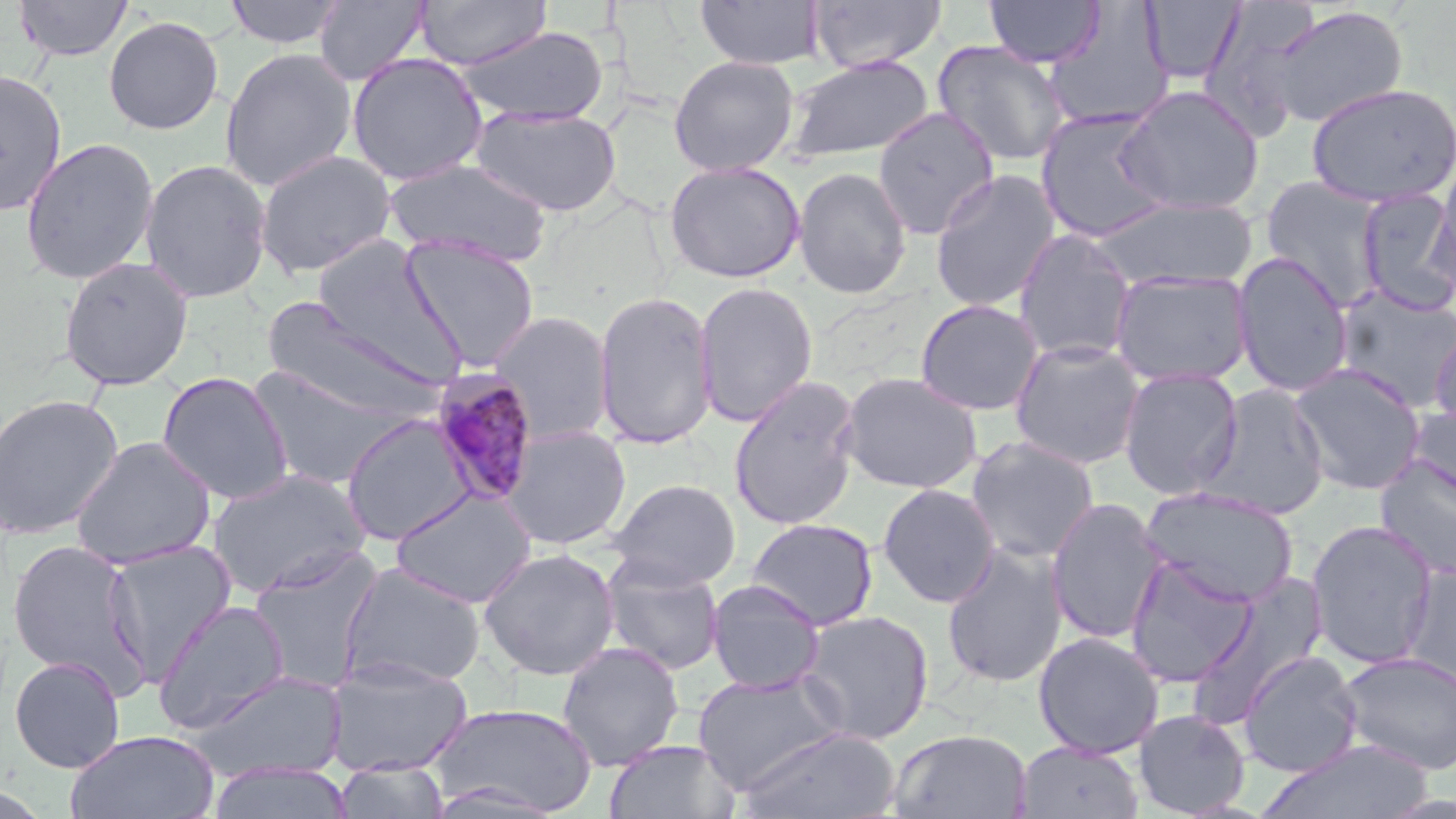
Summary:
  - Coordinate format: approximate bounding boxes as named x1/y1/x2/y2 corners in pixels
  - Plasmodium malariae-infected red blood cell locations: (x1=428, y1=371, x2=542, y2=509)
  - Uninfected red blood cell locations: (x1=13, y1=0, x2=134, y2=62), (x1=224, y1=0, x2=346, y2=50), (x1=313, y1=0, x2=431, y2=86), (x1=694, y1=0, x2=824, y2=70), (x1=809, y1=0, x2=947, y2=73), (x1=984, y1=0, x2=1105, y2=68), (x1=1140, y1=0, x2=1245, y2=86), (x1=416, y1=1, x2=550, y2=70), (x1=1042, y1=4, x2=1174, y2=133), (x1=1261, y1=5, x2=1409, y2=129), (x1=103, y1=15, x2=224, y2=135), (x1=454, y1=26, x2=610, y2=126), (x1=932, y1=40, x2=1072, y2=167), (x1=219, y1=48, x2=358, y2=193), (x1=346, y1=53, x2=489, y2=185), (x1=783, y1=54, x2=935, y2=163), (x1=668, y1=55, x2=799, y2=176), (x1=0, y1=68, x2=67, y2=217), (x1=1305, y1=82, x2=1455, y2=207), (x1=1114, y1=85, x2=1265, y2=216), (x1=469, y1=105, x2=623, y2=217), (x1=873, y1=106, x2=1001, y2=240), (x1=1035, y1=109, x2=1174, y2=242), (x1=20, y1=137, x2=160, y2=286), (x1=255, y1=150, x2=397, y2=278), (x1=383, y1=157, x2=553, y2=267), (x1=139, y1=158, x2=273, y2=304), (x1=1431, y1=159, x2=1456, y2=297), (x1=664, y1=160, x2=805, y2=283), (x1=793, y1=166, x2=912, y2=299), (x1=929, y1=169, x2=1062, y2=313), (x1=1259, y1=176, x2=1389, y2=311), (x1=1356, y1=189, x2=1455, y2=314), (x1=1088, y1=196, x2=1257, y2=292), (x1=1013, y1=229, x2=1139, y2=364), (x1=401, y1=235, x2=541, y2=371), (x1=309, y1=238, x2=464, y2=382), (x1=1231, y1=253, x2=1355, y2=396), (x1=58, y1=256, x2=194, y2=391), (x1=1110, y1=270, x2=1253, y2=389), (x1=694, y1=280, x2=818, y2=428), (x1=1332, y1=285, x2=1456, y2=412), (x1=593, y1=290, x2=718, y2=449), (x1=258, y1=297, x2=449, y2=422), (x1=914, y1=299, x2=1045, y2=416), (x1=487, y1=311, x2=615, y2=444), (x1=1428, y1=324, x2=1456, y2=439), (x1=1009, y1=339, x2=1146, y2=470), (x1=1288, y1=362, x2=1428, y2=496), (x1=244, y1=363, x2=408, y2=491), (x1=1118, y1=367, x2=1243, y2=498), (x1=157, y1=371, x2=295, y2=504), (x1=839, y1=371, x2=983, y2=494), (x1=727, y1=375, x2=863, y2=532), (x1=1197, y1=384, x2=1330, y2=520), (x1=0, y1=393, x2=123, y2=539), (x1=1405, y1=404, x2=1456, y2=507), (x1=341, y1=413, x2=478, y2=546), (x1=500, y1=426, x2=632, y2=550), (x1=965, y1=435, x2=1100, y2=564), (x1=70, y1=437, x2=216, y2=570), (x1=1375, y1=455, x2=1456, y2=578), (x1=206, y1=468, x2=370, y2=598), (x1=607, y1=478, x2=741, y2=589), (x1=877, y1=483, x2=1000, y2=608), (x1=1140, y1=486, x2=1298, y2=607), (x1=390, y1=488, x2=536, y2=608), (x1=1045, y1=497, x2=1168, y2=645), (x1=746, y1=517, x2=878, y2=631), (x1=1305, y1=520, x2=1439, y2=669), (x1=6, y1=538, x2=150, y2=693), (x1=101, y1=540, x2=237, y2=680), (x1=941, y1=543, x2=1067, y2=688), (x1=248, y1=546, x2=384, y2=693), (x1=478, y1=547, x2=620, y2=681), (x1=1125, y1=556, x2=1258, y2=688), (x1=599, y1=557, x2=725, y2=675), (x1=339, y1=562, x2=486, y2=689), (x1=1400, y1=563, x2=1456, y2=692), (x1=1187, y1=571, x2=1331, y2=723), (x1=706, y1=580, x2=826, y2=695), (x1=154, y1=600, x2=291, y2=733), (x1=797, y1=609, x2=935, y2=745), (x1=1033, y1=631, x2=1165, y2=759), (x1=556, y1=641, x2=684, y2=770), (x1=1336, y1=650, x2=1456, y2=775), (x1=1238, y1=651, x2=1364, y2=778), (x1=9, y1=655, x2=125, y2=773), (x1=324, y1=657, x2=474, y2=777), (x1=692, y1=670, x2=848, y2=794), (x1=191, y1=671, x2=349, y2=783), (x1=428, y1=702, x2=599, y2=816), (x1=1132, y1=708, x2=1251, y2=818), (x1=736, y1=727, x2=901, y2=818), (x1=886, y1=728, x2=1033, y2=819), (x1=65, y1=730, x2=219, y2=819), (x1=604, y1=739, x2=741, y2=819), (x1=1258, y1=739, x2=1436, y2=818), (x1=1015, y1=741, x2=1145, y2=818), (x1=332, y1=759, x2=452, y2=819)
  - Slide-level diagnosis: Plasmodium malariae
  - Stain: May-Grünwald-Giemsa
  - Image size: 1456×819 pixels
  - Preparation: thin blood smear
  - Magnification: 1000x
  - Modality: light microscopy
  - Field of view: one of a larger specimen